Locate and identify every blood parasite.
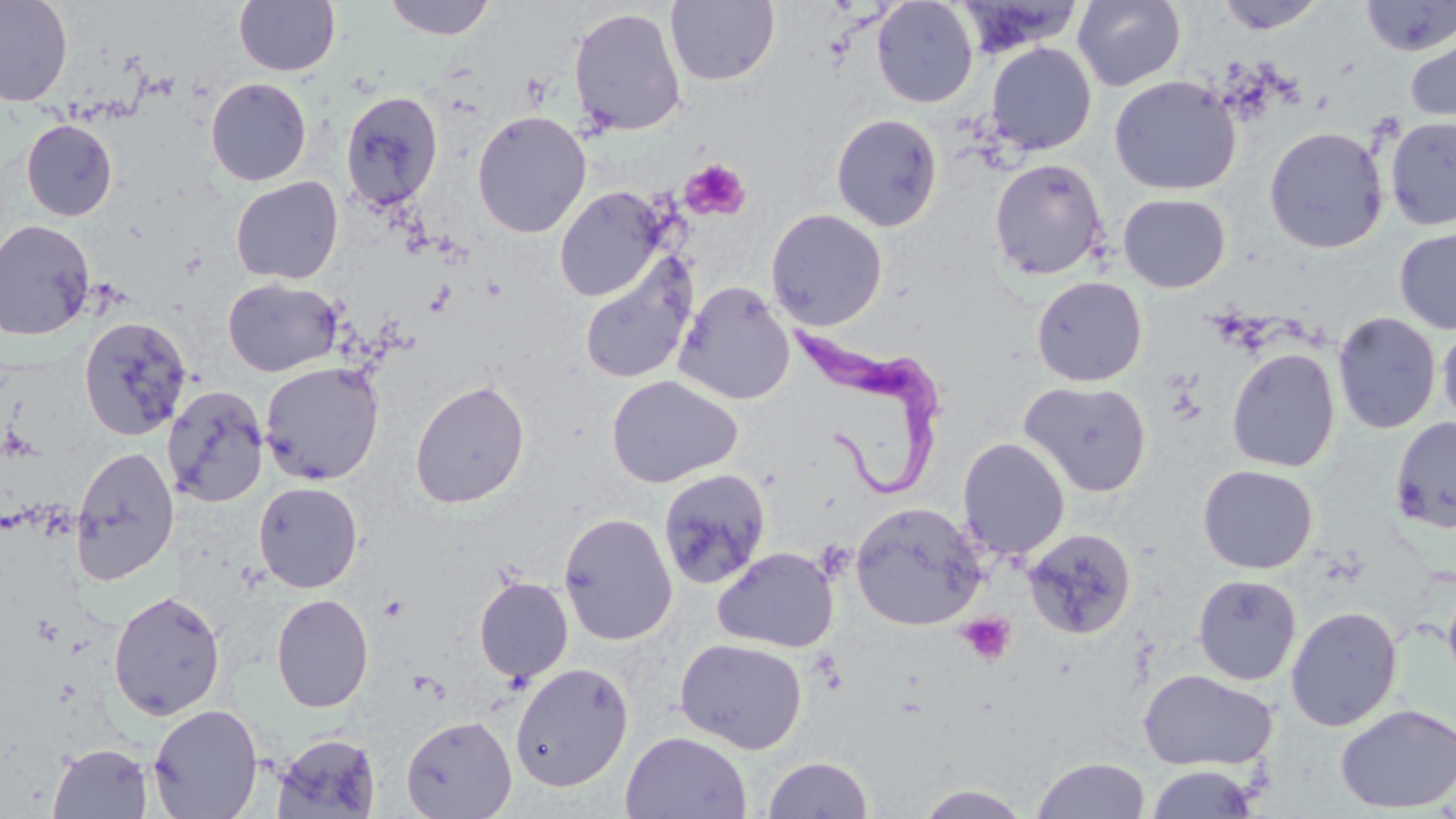

Approximate bounding boxes as named x1/y1/x2/y2 corners in pixels.
Trypanosoma brucei: (x1=786, y1=320, x2=948, y2=501).
No Plasmodium falciparum, Plasmodium ovale, Plasmodium malariae, Plasmodium vivax, or Babesia divergens observed.

Uninfected red blood cell locations: (x1=0, y1=0, x2=73, y2=107), (x1=233, y1=0, x2=341, y2=77), (x1=383, y1=0, x2=496, y2=40), (x1=665, y1=0, x2=780, y2=86), (x1=871, y1=0, x2=979, y2=108), (x1=1215, y1=0, x2=1327, y2=34), (x1=1361, y1=0, x2=1456, y2=56), (x1=957, y1=1, x2=1083, y2=58), (x1=1073, y1=1, x2=1186, y2=90), (x1=569, y1=7, x2=687, y2=137), (x1=1404, y1=30, x2=1456, y2=133), (x1=985, y1=42, x2=1097, y2=155), (x1=1109, y1=75, x2=1241, y2=196), (x1=205, y1=77, x2=312, y2=186), (x1=340, y1=90, x2=444, y2=212), (x1=471, y1=110, x2=591, y2=238), (x1=831, y1=114, x2=943, y2=232), (x1=1384, y1=117, x2=1456, y2=231), (x1=21, y1=119, x2=118, y2=221), (x1=1264, y1=126, x2=1388, y2=254), (x1=989, y1=158, x2=1109, y2=281), (x1=230, y1=176, x2=344, y2=285), (x1=554, y1=186, x2=669, y2=302), (x1=1118, y1=193, x2=1231, y2=293), (x1=766, y1=208, x2=888, y2=330), (x1=0, y1=219, x2=96, y2=340), (x1=1394, y1=226, x2=1456, y2=335), (x1=579, y1=256, x2=698, y2=385), (x1=1031, y1=276, x2=1147, y2=387), (x1=223, y1=277, x2=343, y2=377), (x1=673, y1=281, x2=795, y2=406), (x1=1332, y1=312, x2=1441, y2=434), (x1=79, y1=316, x2=193, y2=440), (x1=1437, y1=322, x2=1456, y2=431), (x1=1226, y1=348, x2=1340, y2=473), (x1=260, y1=362, x2=384, y2=485), (x1=606, y1=375, x2=743, y2=488), (x1=410, y1=379, x2=530, y2=509), (x1=1020, y1=379, x2=1152, y2=497), (x1=162, y1=386, x2=268, y2=508), (x1=1389, y1=416, x2=1456, y2=534), (x1=957, y1=437, x2=1070, y2=560), (x1=70, y1=445, x2=179, y2=585), (x1=1197, y1=464, x2=1318, y2=574), (x1=657, y1=469, x2=771, y2=589), (x1=253, y1=481, x2=364, y2=594), (x1=849, y1=501, x2=987, y2=631), (x1=558, y1=511, x2=678, y2=645), (x1=1023, y1=527, x2=1137, y2=640), (x1=712, y1=546, x2=839, y2=653), (x1=1192, y1=574, x2=1302, y2=686), (x1=1442, y1=574, x2=1456, y2=696), (x1=474, y1=576, x2=574, y2=684), (x1=107, y1=589, x2=226, y2=721), (x1=271, y1=593, x2=374, y2=713), (x1=1286, y1=605, x2=1403, y2=731), (x1=674, y1=637, x2=808, y2=754), (x1=509, y1=661, x2=634, y2=792), (x1=1138, y1=669, x2=1278, y2=771), (x1=1334, y1=703, x2=1456, y2=814), (x1=148, y1=704, x2=264, y2=818), (x1=401, y1=715, x2=516, y2=819), (x1=620, y1=731, x2=752, y2=818), (x1=271, y1=732, x2=382, y2=817), (x1=48, y1=743, x2=153, y2=819), (x1=761, y1=755, x2=875, y2=819), (x1=1031, y1=756, x2=1150, y2=818), (x1=1143, y1=764, x2=1264, y2=818), (x1=912, y1=783, x2=1036, y2=818). Platelet locations: (x1=681, y1=158, x2=751, y2=221), (x1=957, y1=613, x2=1016, y2=666). Slide-level diagnosis: Trypanosoma brucei. Thin blood smear. Single field of view. Optical microscopy. Captured at 1000x magnification. Image is 1456×819 pixels. May-Grünwald-Giemsa-stained preparation.